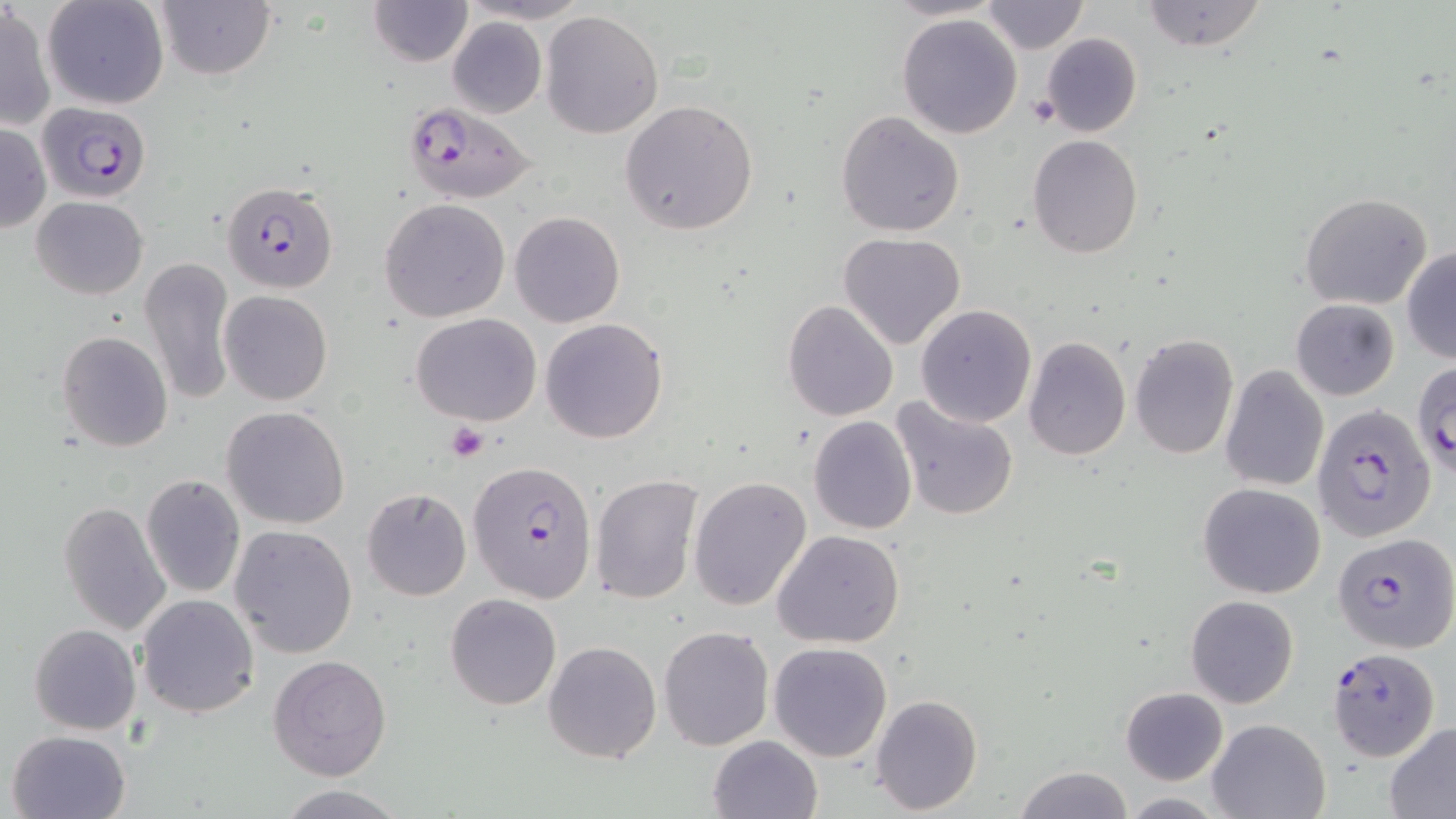
slide-level diagnosis = Plasmodium falciparum
image size = 1456×819 pixels
modality = optical microscopy
stain = May-Grünwald-Giemsa
platelet locations = approximate bounding boxes as (x1, y1, x2, y2) in pixels: (1028, 95, 1061, 125), (445, 422, 490, 462)
magnification = 1000x
preparation = thin blood film
field of view = one of a larger specimen
uninfected red blood cell locations = approximate bounding boxes as (x1, y1, x2, y2) in pixels: (42, 0, 168, 110), (154, 0, 275, 79), (370, 0, 472, 67), (462, 0, 591, 24), (978, 0, 1089, 53), (1139, 0, 1268, 51), (1, 3, 55, 132), (541, 10, 666, 139), (896, 13, 1023, 139), (446, 16, 546, 118), (1039, 32, 1143, 139), (620, 99, 759, 234), (836, 110, 965, 238), (0, 123, 49, 233), (1028, 135, 1143, 258), (1300, 192, 1433, 310), (32, 195, 149, 299), (380, 198, 511, 321), (509, 210, 626, 327), (838, 232, 967, 350), (1403, 247, 1456, 365), (140, 256, 236, 406), (218, 291, 334, 406), (1290, 298, 1400, 401), (783, 299, 898, 421), (915, 304, 1037, 427), (410, 312, 542, 426), (541, 317, 669, 443), (57, 330, 173, 454), (1129, 334, 1240, 460), (1024, 336, 1132, 460), (1219, 364, 1330, 492), (891, 396, 1021, 522), (221, 406, 351, 530), (807, 415, 918, 535), (140, 475, 245, 597), (591, 475, 704, 605), (690, 477, 812, 613), (1197, 482, 1327, 599), (361, 487, 471, 601), (58, 500, 171, 638), (229, 526, 359, 659), (772, 529, 905, 648), (446, 592, 562, 710), (136, 594, 259, 718), (1186, 594, 1298, 708), (29, 624, 142, 735), (658, 626, 775, 750), (543, 640, 661, 763), (769, 642, 893, 763), (268, 655, 393, 781), (1120, 686, 1229, 785), (870, 694, 983, 816), (1206, 718, 1332, 818), (1383, 722, 1456, 816), (6, 730, 132, 819), (708, 734, 823, 819), (1012, 765, 1133, 819), (274, 785, 411, 818), (1116, 794, 1229, 818)
Plasmodium falciparum-infected red blood cell locations = approximate bounding boxes as (x1, y1, x2, y2) in pixels: (37, 100, 153, 202), (401, 101, 538, 205), (225, 183, 341, 296), (1413, 356, 1456, 476), (1313, 404, 1437, 543), (468, 459, 599, 602), (1332, 532, 1456, 655), (1326, 649, 1440, 764)